Identify the parasite.
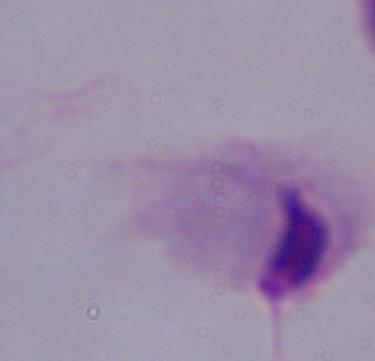

A trichomonad.

1000x magnification. Photomicrograph.